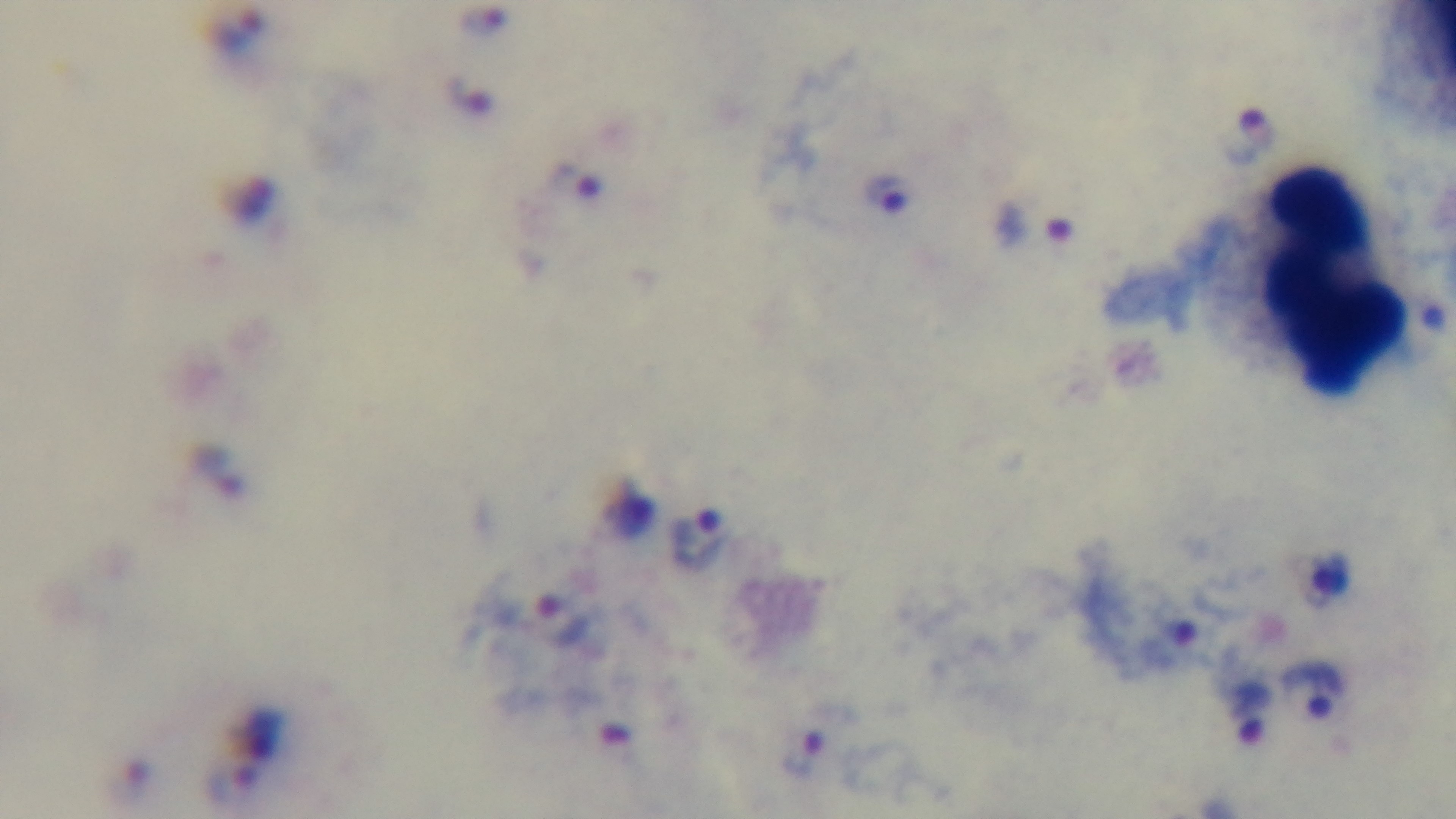
{
  "objective": "100x oil immersion",
  "field_of_view": "single",
  "modality": "light microscopy",
  "stain": "Giemsa",
  "preparation": "thick blood film",
  "malaria_status": "positive",
  "capture": "mounted 4K digital camera"
}